Identify the cell.
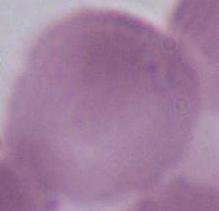
An erythrocyte.

Summary:
  - Modality: photomicrograph
  - Magnification: 1000x